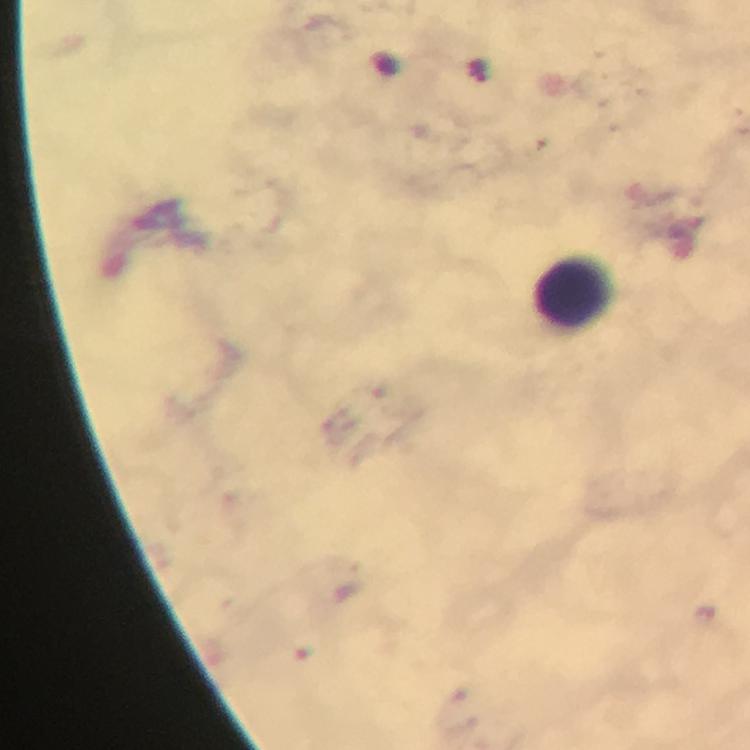
preparation = thick blood smear
cropped from = a single field of view
stain = Giemsa
magnification = 100x
immersion oil = used
context = from a diagnostic examination for malaria
image size = 750×750 pixels
Plasmodium parasites = none detected
leukocyte locations = approximate centers as [x, y] in pixels: [573, 293]
capture = smartphone photograph through a microscope